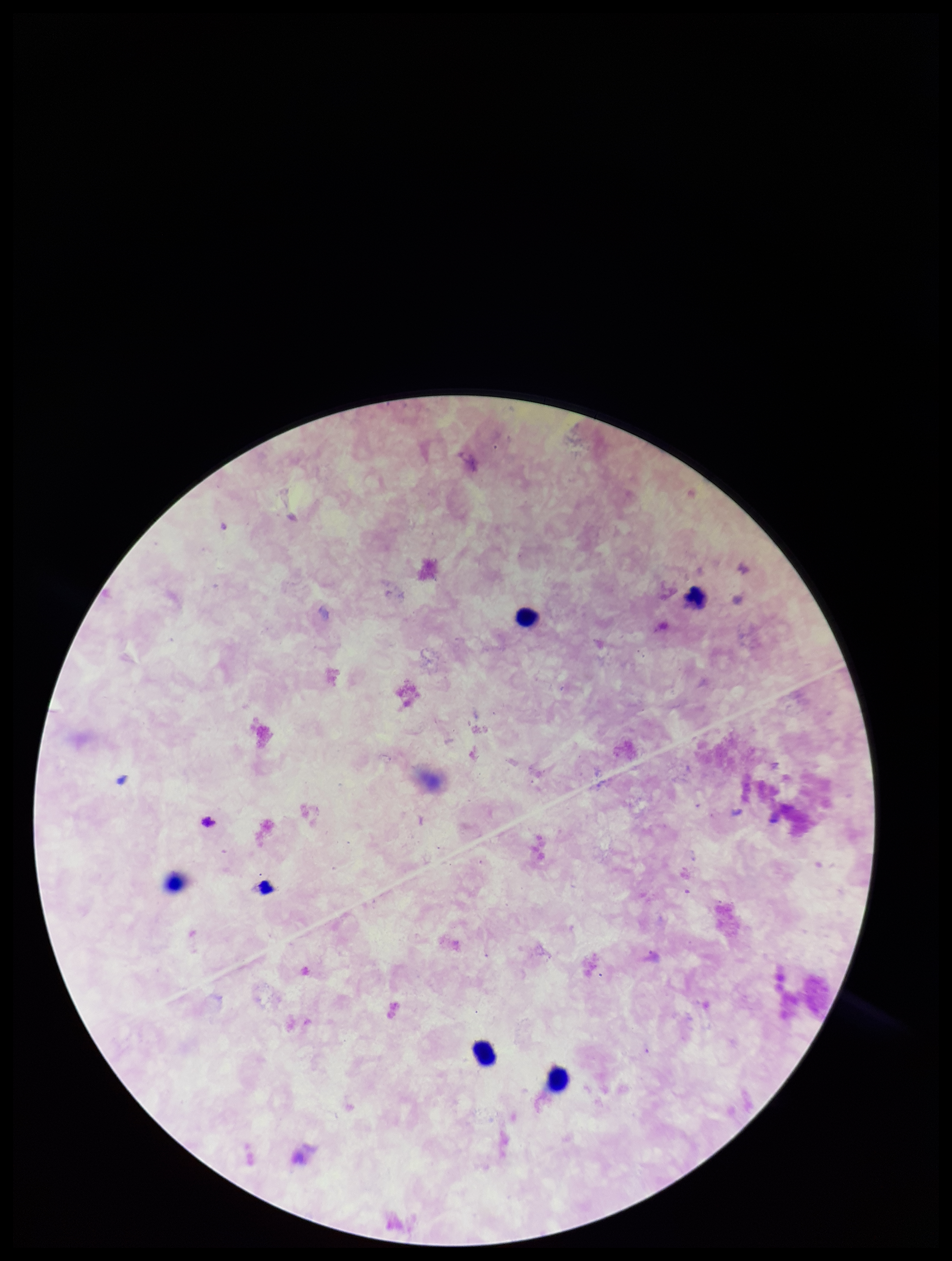

preparation: thick blood smear
field_of_view: single
patient_malaria_status: negative
leukocyte_count: 4
image_size: 952×1261 pixels
parasite_count: 0
capture: smartphone photograph through the microscope eyepiece
stain: Giemsa
plasmodium_parasites: none detected